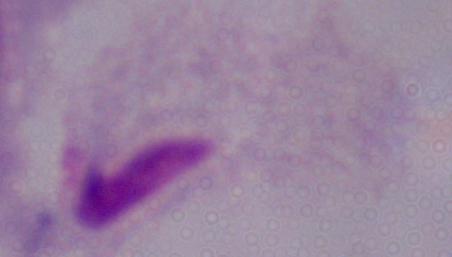
Micrograph. 1000x magnification. A trichomonad is seen.